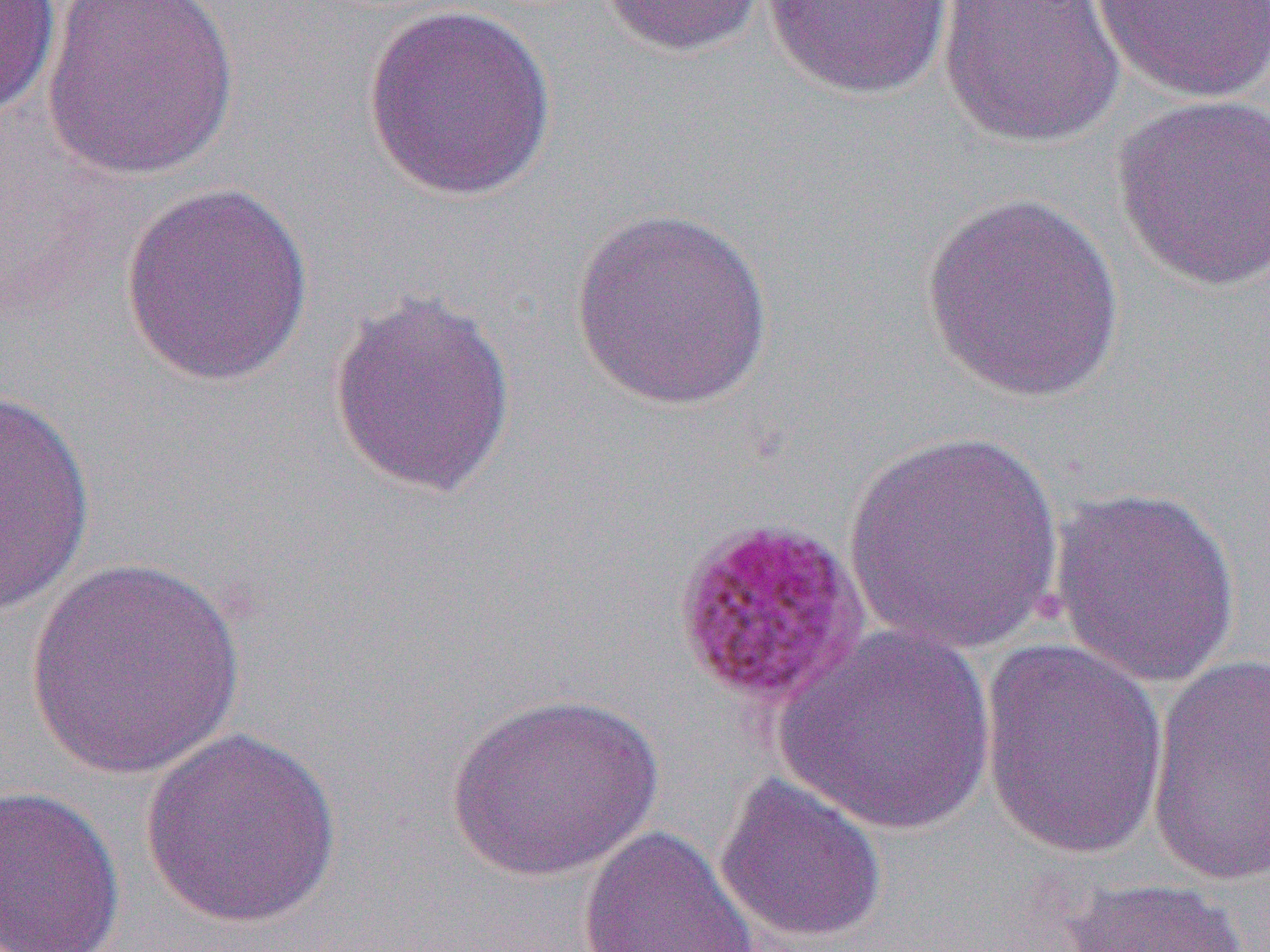
Summary:
  - Coordinate format: approximate bounding boxes as [x1, y1, x2, y2] in pixels
  - Plasmodium malariae-infected red blood cell locations: [668, 513, 871, 710]
  - Uninfected red blood cell locations: [0, 0, 63, 119], [43, 0, 240, 182], [598, 0, 771, 58], [1092, 0, 1270, 103], [762, 1, 955, 100], [936, 1, 1126, 149], [361, 3, 558, 202], [1110, 93, 1270, 292], [119, 181, 315, 388], [919, 193, 1127, 403], [569, 206, 777, 411], [325, 289, 518, 500], [0, 386, 96, 619], [845, 429, 1066, 657], [1049, 484, 1244, 688], [22, 557, 249, 781], [776, 625, 998, 835], [978, 639, 1169, 858], [1146, 651, 1270, 890], [443, 691, 665, 883], [137, 726, 344, 930], [713, 772, 888, 945], [0, 784, 126, 951], [578, 825, 760, 952], [1060, 876, 1252, 952]
  - Slide-level diagnosis: Plasmodium malariae
  - Field of view: one of a larger specimen
  - Preparation: thin blood smear
  - Magnification: 1000x
  - Image size: 1270×952 pixels
  - Modality: optical microscopy